Evaluate for malaria.
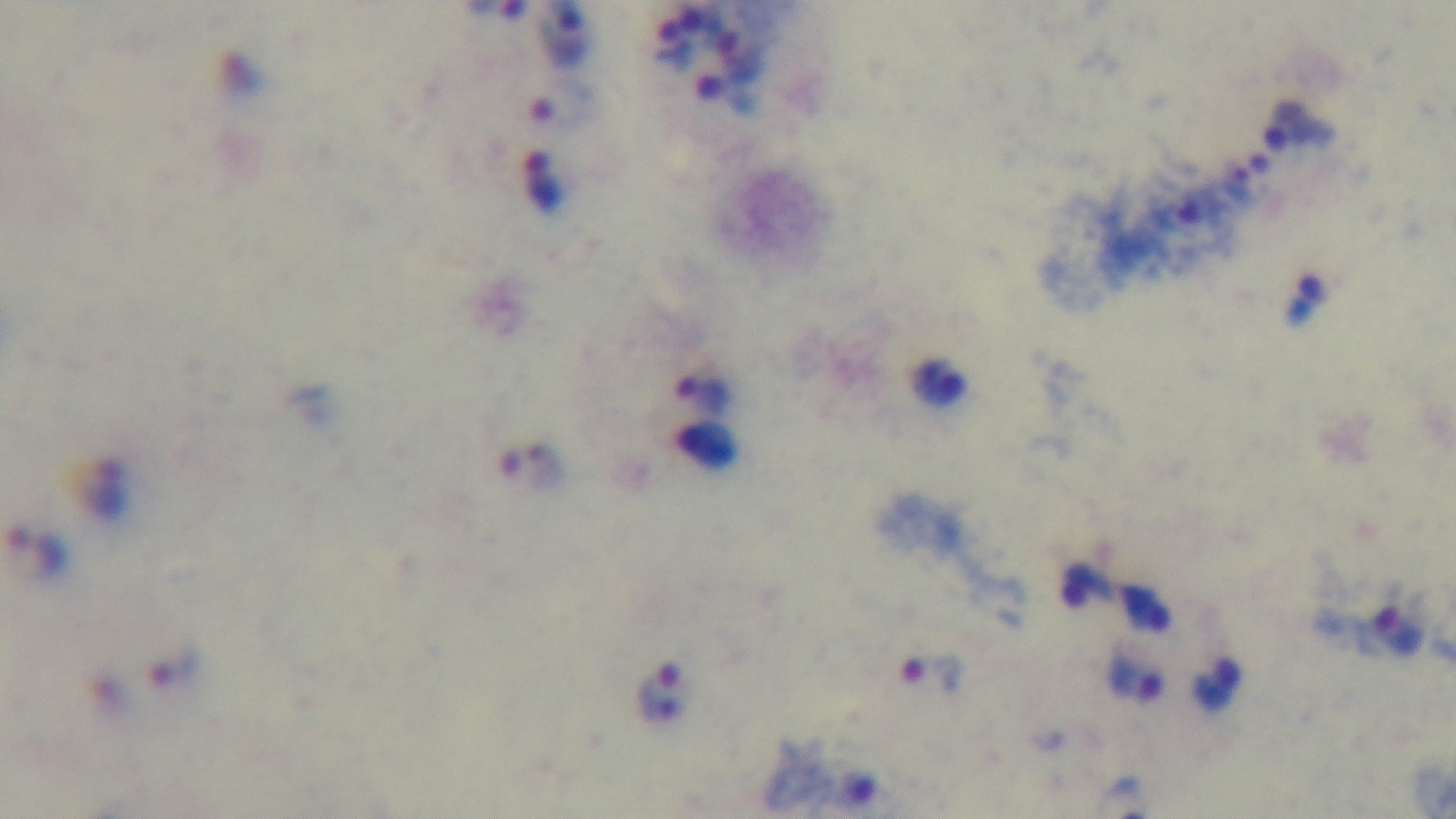

It is infected.

Summary:
  - Capture: mounted 4K digital camera
  - Objective: 100x oil immersion
  - Preparation: thick blood film
  - Field of view: one from the slide
  - Stain: Giemsa
  - Modality: light microscopy